Identify the parasite.
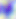

Toxoplasma gondii.

modality: photomicrograph
magnification: 400x